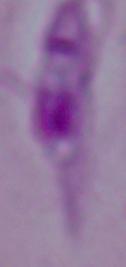
identification = Leishmania
magnification = 1000x
modality = micrograph